Point out each leukocyte.
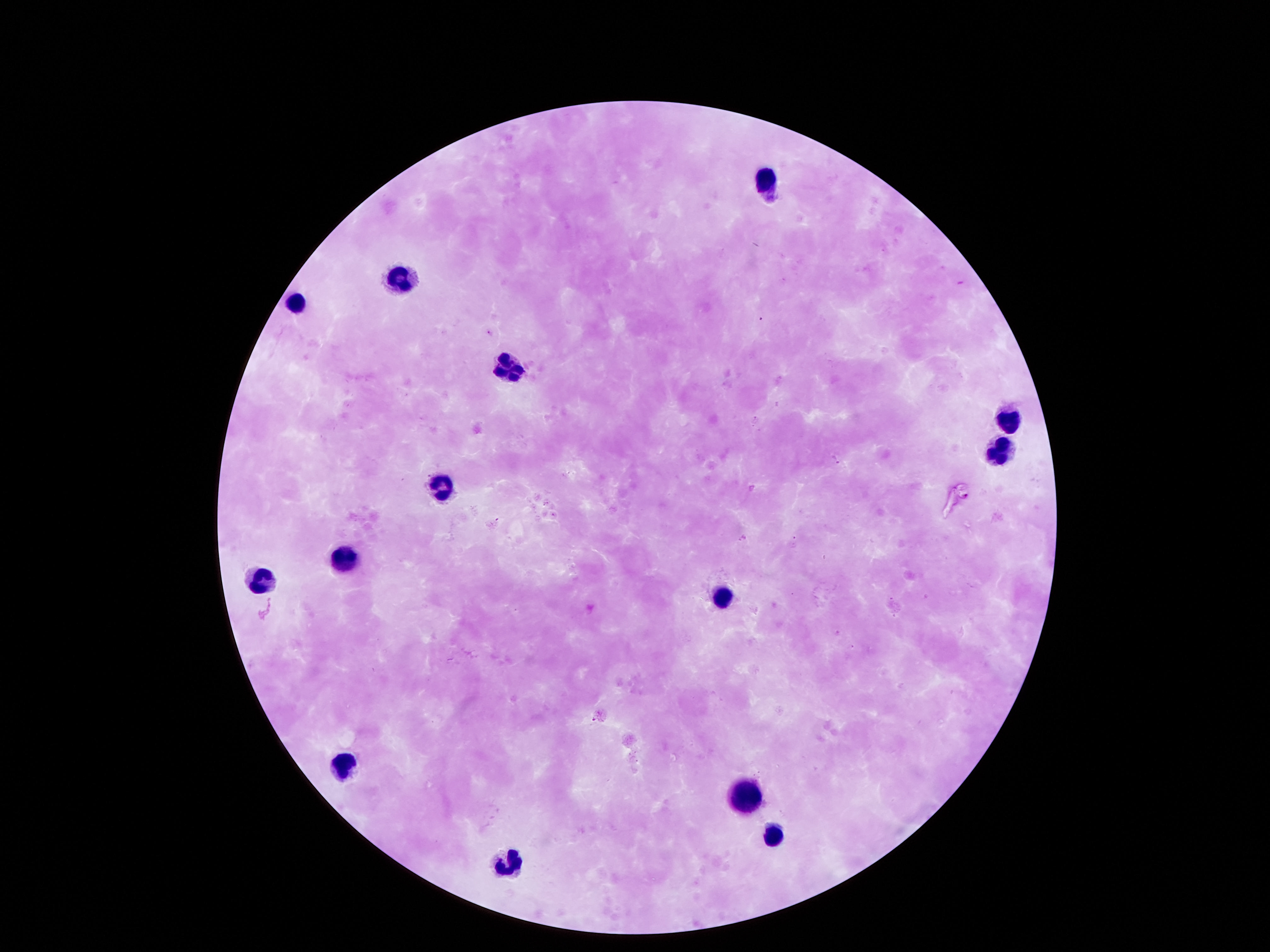
Approximate centers as [x, y] in pixels.
Leukocytes: [761, 177], [396, 273], [299, 299], [503, 364], [1007, 421], [1000, 451], [445, 483], [348, 554], [257, 577], [719, 592], [345, 761], [745, 789], [774, 834], [509, 861].

field of view = single
stain = Giemsa
preparation = thick blood film
magnification = 100x
capture = smartphone camera through the microscope eyepiece
patient malaria status = not infected
image size = 1270×952 pixels